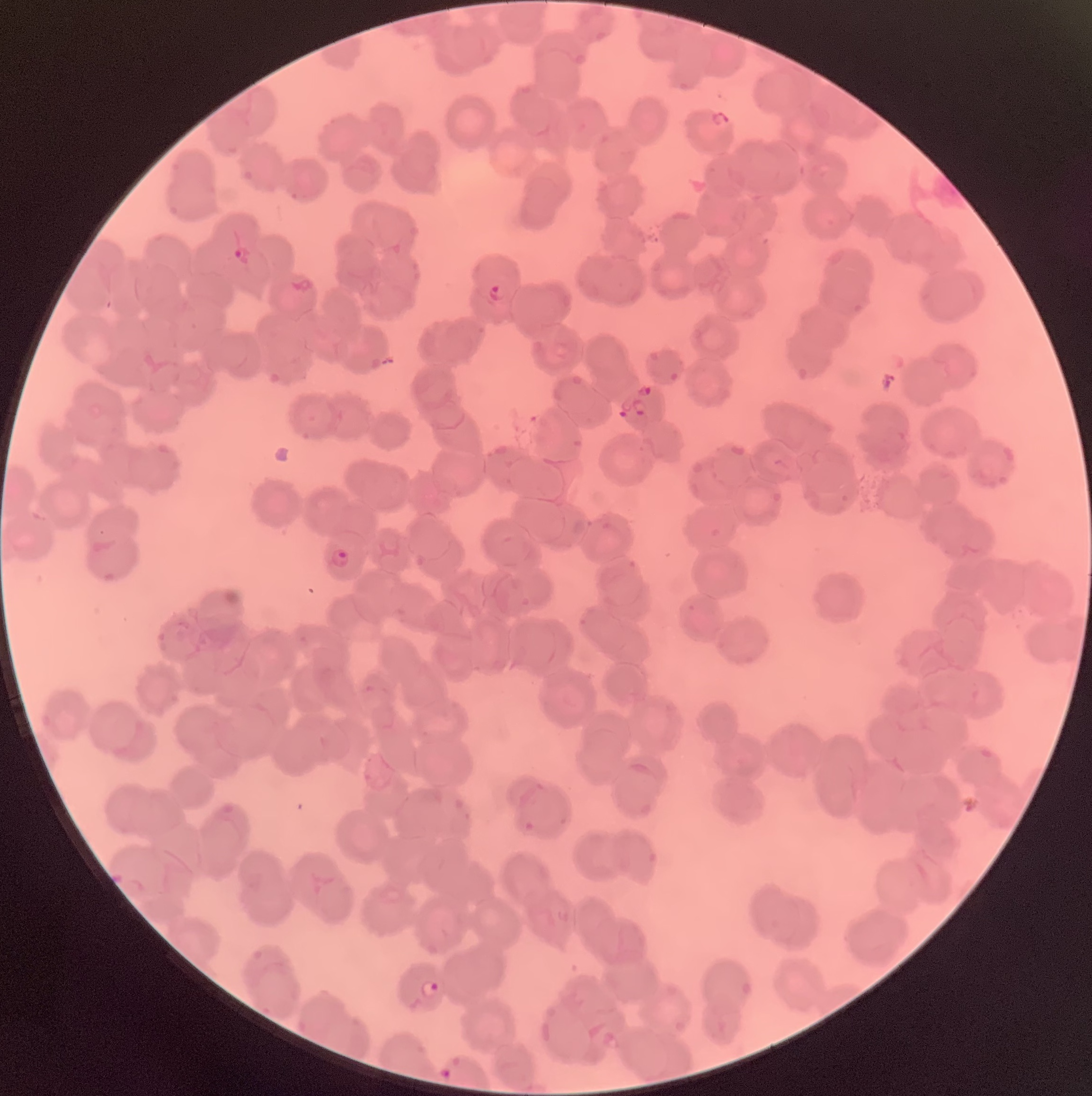
{
  "plasmodium_parasite_locations": "approximate bounding boxes as named x1/y1/x2/y2 corners in pixels: (x1=711, y1=108, x2=729, y2=130), (x1=234, y1=245, x2=253, y2=264), (x1=486, y1=283, x2=507, y2=301), (x1=637, y1=383, x2=653, y2=396), (x1=632, y1=399, x2=647, y2=417), (x1=618, y1=401, x2=632, y2=417), (x1=330, y1=547, x2=352, y2=568), (x1=418, y1=979, x2=440, y2=998), (x1=438, y1=1066, x2=455, y2=1082)",
  "modality": "optical microscopy",
  "red_blood_cell_morphology": "rouleaux formation",
  "preparation": "thin blood smear",
  "image_size": "1092×1096 pixels"
}